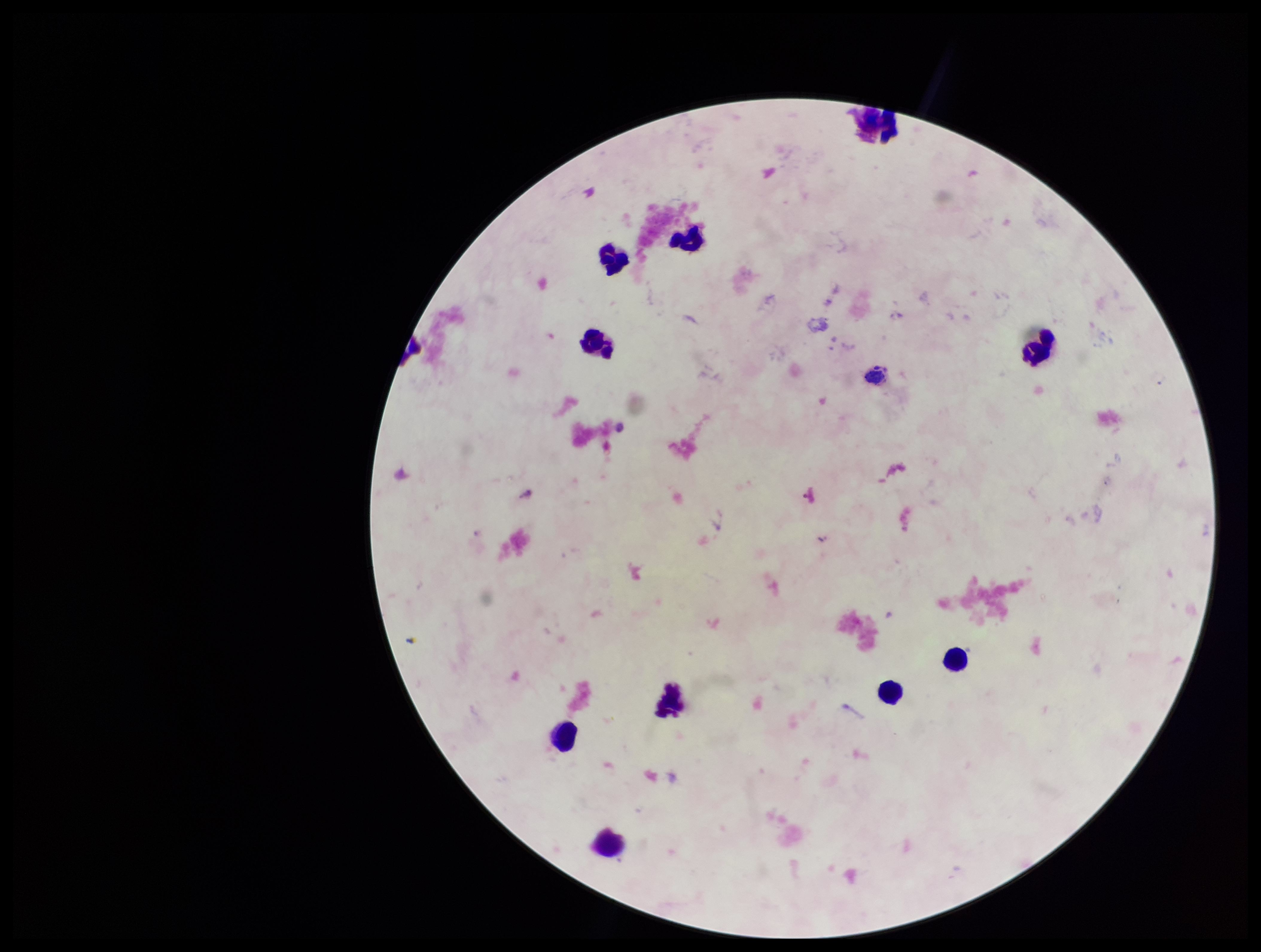
{
  "capture": "smartphone photograph through the microscope eyepiece",
  "parasite_count": 0,
  "plasmodium_parasites": "none seen",
  "leukocyte_count": 10,
  "patient_malaria_status": "negative",
  "preparation": "thick",
  "image_size": "1261×952 pixels",
  "stain": "Giemsa",
  "field_of_view": "one from this slide"
}